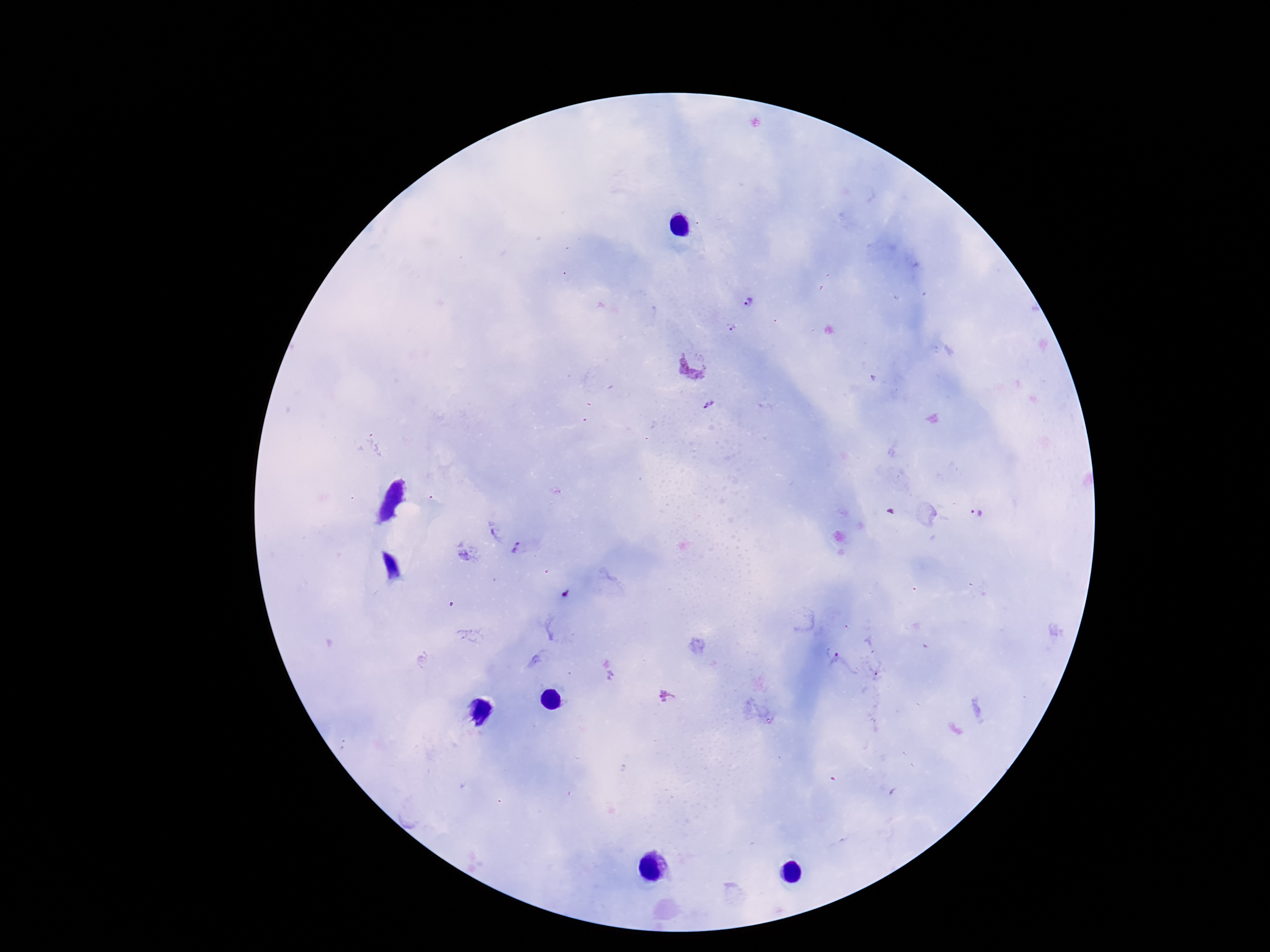

Approximate object centers, in pixels from the top-left corner.
Summary:
  - Plasmodium parasite locations: (x=750, y=302), (x=732, y=327), (x=695, y=361), (x=710, y=403), (x=975, y=515), (x=519, y=551), (x=566, y=594), (x=836, y=659)
  - Stain: Giemsa
  - Image size: 1270×952 pixels
  - Capture: smartphone camera through the microscope eyepiece
  - Magnification: 100x
  - Field of view: one from this slide
  - Patient malaria status: infected
  - Preparation: thick blood smear